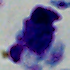

magnification: 1000x
identification: leukocyte
modality: photomicrograph